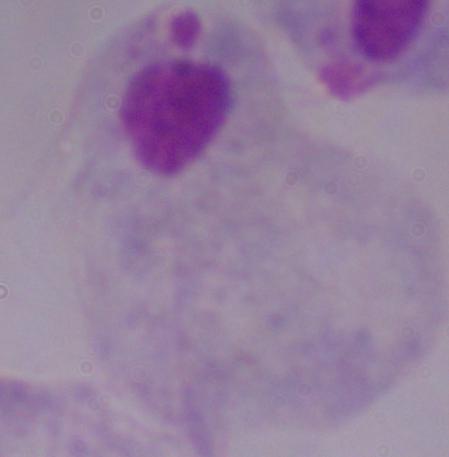

magnification: 1000x
identification: trichomonad
modality: photomicrograph